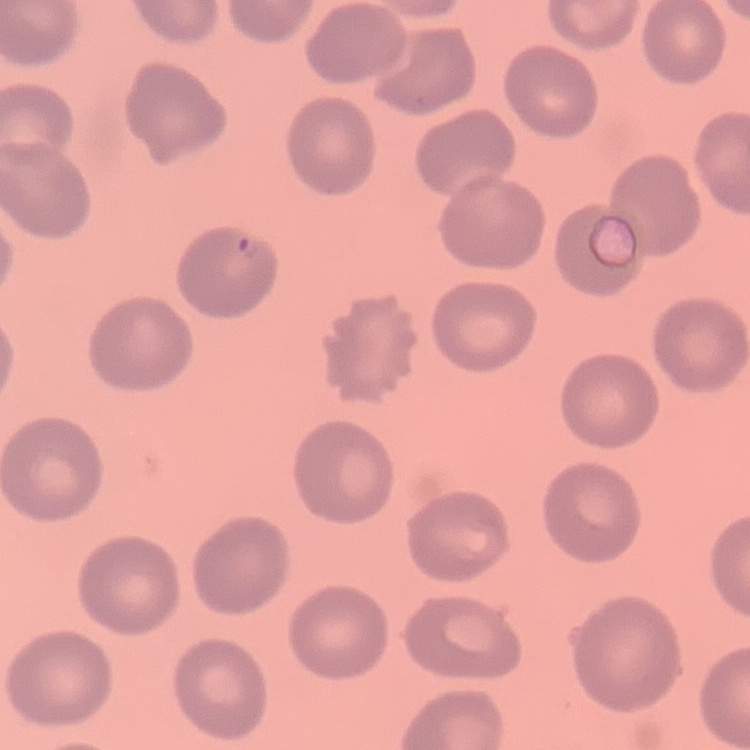
erythrocyte_morphology: no rouleaux formation
stain: Field's or Giemsa
preparation: thin blood film
image_type: one tile cut from a larger photomicrograph